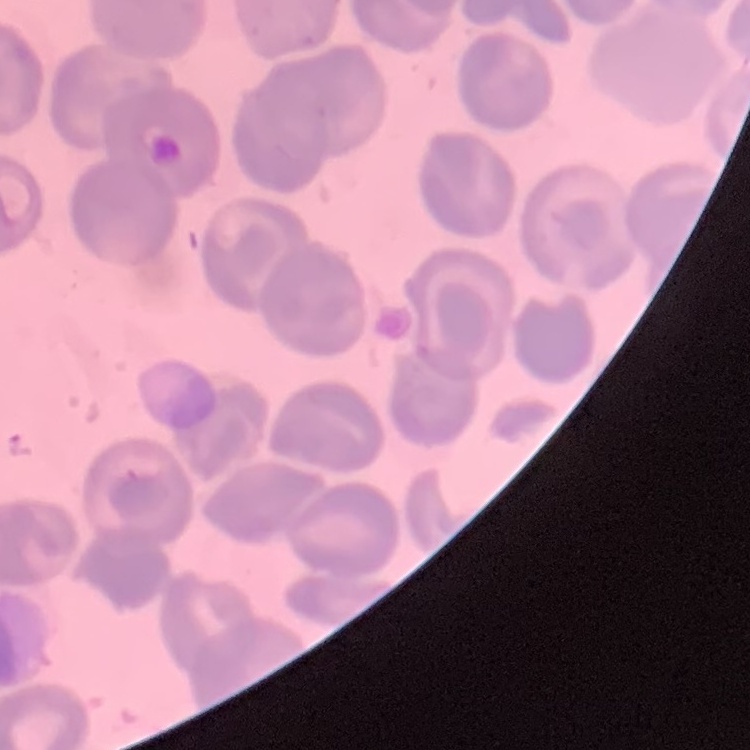

erythrocyte morphology = no rouleaux formation
stain = Field's or Giemsa
image type = square crop of a larger photomicrograph
preparation = thin blood film